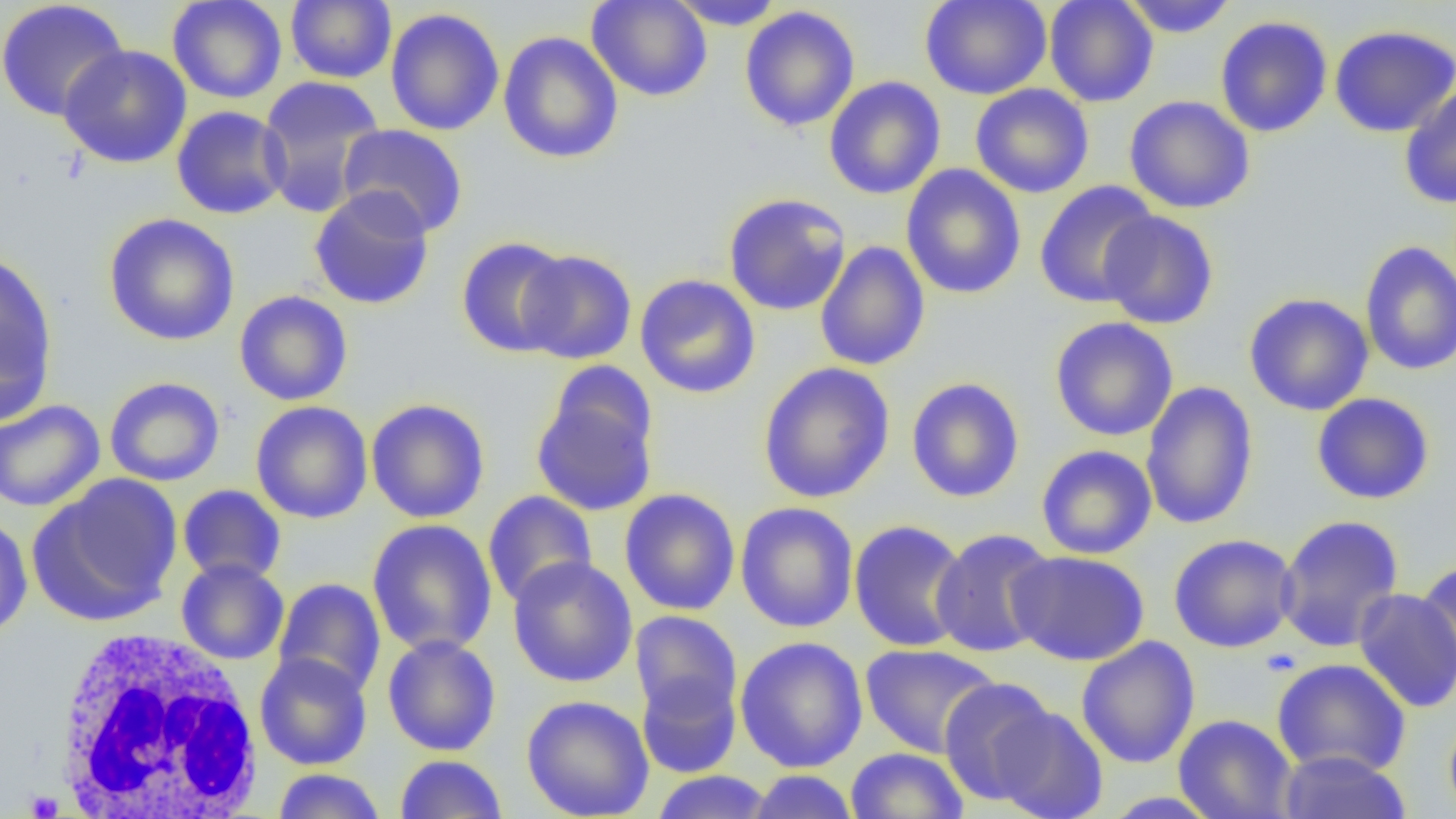

Summary:
  - Coordinate format: approximate bounding boxes as (x1,y1)-(x2,y2) corner pairs in pixels
  - Platelet locations: (23,790)-(64,817)
  - White blood cell locations: (47,625)-(265,819)
  - Uninfected red blood cell locations: (167,0)-(287,104), (586,0)-(713,102), (668,0)-(786,30), (919,0)-(1052,100), (1043,0)-(1159,107), (1119,0)-(1238,38), (286,1)-(397,84), (0,2)-(130,122), (739,6)-(860,132), (385,8)-(505,136), (1214,15)-(1333,138), (1329,24)-(1456,138), (498,32)-(624,164), (58,44)-(193,168), (256,76)-(386,217), (823,76)-(946,200), (970,84)-(1095,198), (1399,85)-(1456,210), (1124,95)-(1255,214), (171,105)-(291,220), (336,123)-(469,237), (900,164)-(1027,300), (1034,181)-(1160,308), (308,186)-(436,310), (722,193)-(852,316), (1098,210)-(1219,330), (103,213)-(240,347), (456,236)-(574,357), (1359,240)-(1456,377), (814,241)-(930,371), (517,249)-(637,365), (0,250)-(58,419), (634,274)-(761,399), (234,290)-(353,406), (1244,292)-(1374,416), (1049,317)-(1179,441), (545,359)-(659,464), (757,361)-(896,503), (104,376)-(225,487), (906,377)-(1025,503), (1140,381)-(1259,530), (531,387)-(659,517), (1311,392)-(1436,505), (365,397)-(490,524), (0,399)-(106,512), (250,401)-(373,524), (1036,445)-(1157,560), (28,473)-(182,626), (177,485)-(286,585), (620,488)-(740,616), (482,490)-(598,608), (735,502)-(859,633), (1276,514)-(1405,653), (0,515)-(33,640), (367,518)-(498,657), (848,520)-(970,652), (930,528)-(1058,658), (1168,533)-(1300,653), (1007,549)-(1150,666), (508,556)-(638,688), (176,559)-(289,665), (1415,562)-(1456,684), (273,578)-(386,698), (1352,587)-(1455,713), (630,610)-(743,722), (382,635)-(501,757), (735,635)-(868,773), (1076,635)-(1200,768), (860,643)-(1001,758), (254,652)-(373,770), (1271,657)-(1411,778), (636,670)-(741,779), (938,676)-(1060,806), (521,694)-(654,819), (988,704)-(1109,819), (1444,710)-(1456,819), (1173,714)-(1298,819), (845,747)-(968,819), (1276,749)-(1412,819), (395,754)-(508,819), (272,768)-(386,819), (650,770)-(775,819), (745,770)-(860,819), (1098,791)-(1223,818)
  - Slide-level diagnosis: no evidence of blood parasites
  - Preparation: thin blood smear
  - Image size: 1456×819 pixels
  - Magnification: 1000x
  - Field of view: single
  - Modality: optical microscopy